Assess this cell for malaria.
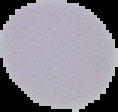

It is uninfected.

The area outside the segmented cell region is set to black. Image is 118×112 pixels. From a thin blood film.